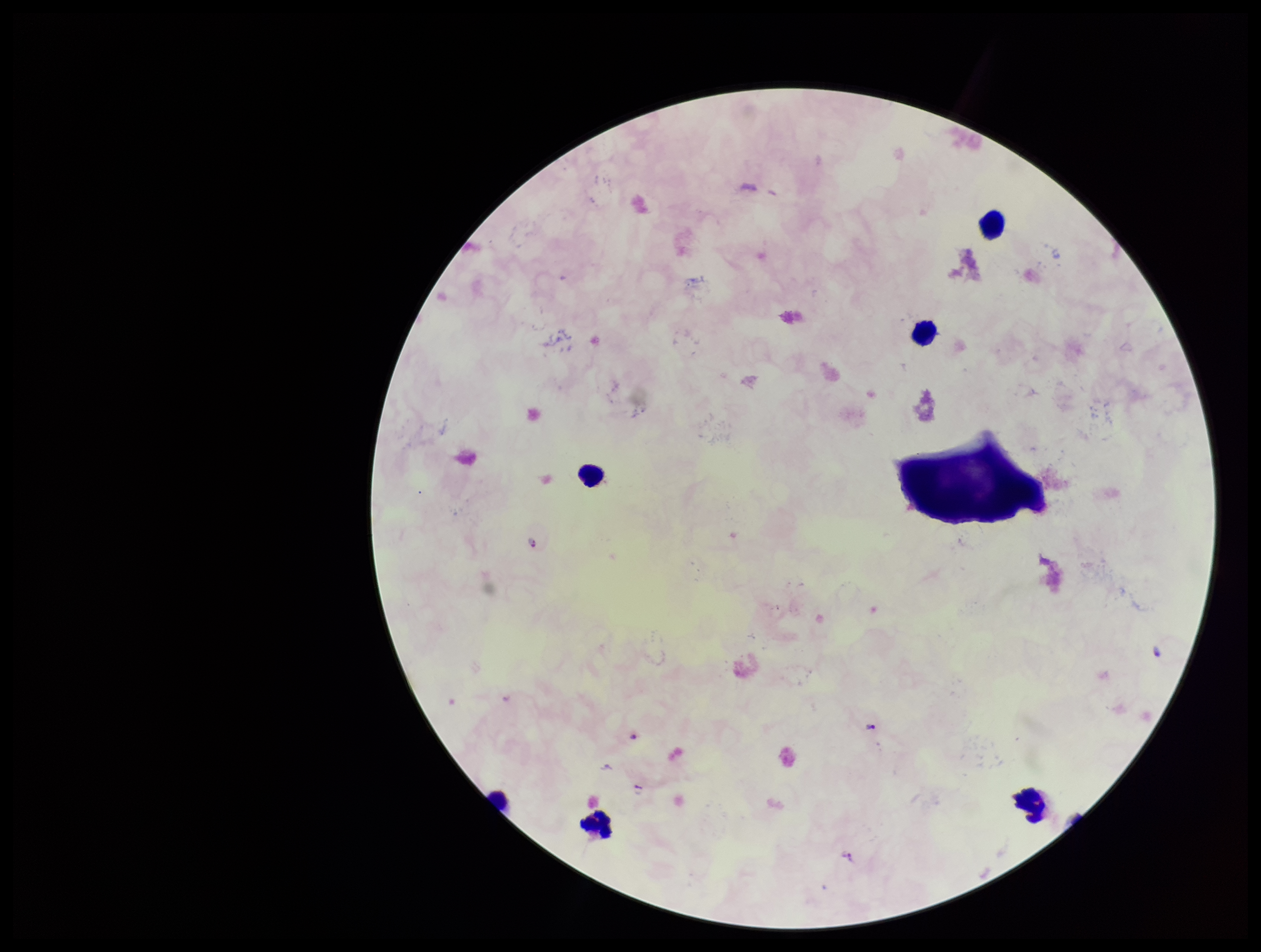

Preparation: thick smear. One field from this slide. Species reported for this patient: Plasmodium falciparum. Plasmodium parasites: identified. Image is 1261×952 pixels. Photographed through the microscope eyepiece with a smartphone camera. Patient malaria status: infected. Leukocyte count: 6. Parasite count: 3. Giemsa stain.